Classify this cell by malaria status.
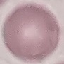
Uninfected.

Cell patch, automatically extracted from a larger field of view and resized to 64 × 64 pixels. Giemsa stain. Thin blood smear. Acquired by smartphone through the microscope eyepiece.